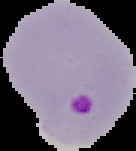

result = Plasmodium parasites identified
preparation = thin blood smear
image type = segmented cell region with the area outside set to black
image size = 136×151 pixels